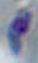

modality: micrograph
magnification: 1000x
identification: Toxoplasma gondii